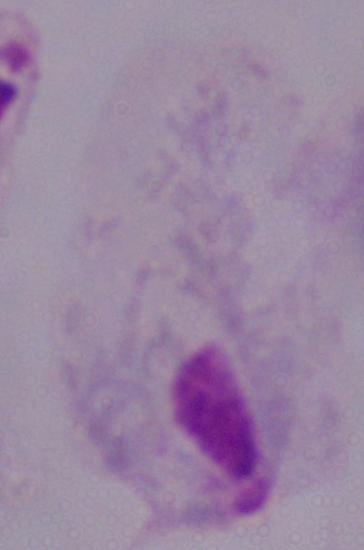

modality = micrograph
identification = trichomonad
magnification = 1000x